Report the malaria status of this cell.
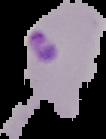

It is parasitized.

image type = cell region segmented out of the field of view; surrounding area masked to black
preparation = thin blood film
image size = 106×139 pixels